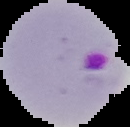

malaria status = parasitized
preparation = thin blood smear
image type = segmented cell region on a black background
image size = 130×127 pixels